Comment on the morphology of the erythrocytes.
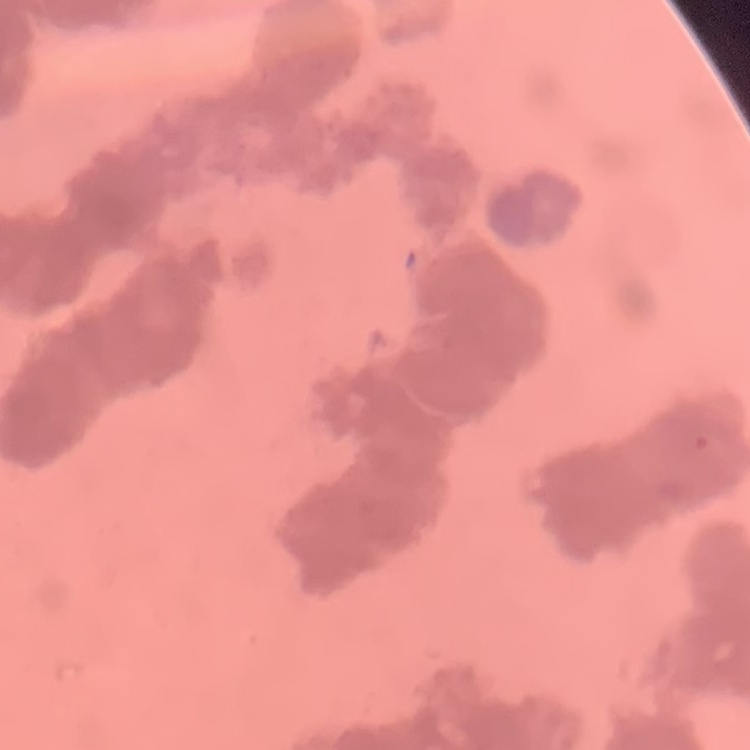
They show rouleaux formation.

{
  "preparation": "thin blood smear",
  "stain": "Field's or Giemsa",
  "image_type": "square crop of a larger photomicrograph"
}